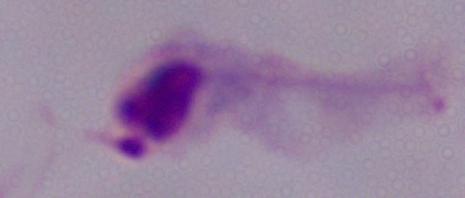 1000x magnification. Micrograph. A trichomonad is shown.